Give the preparation type.
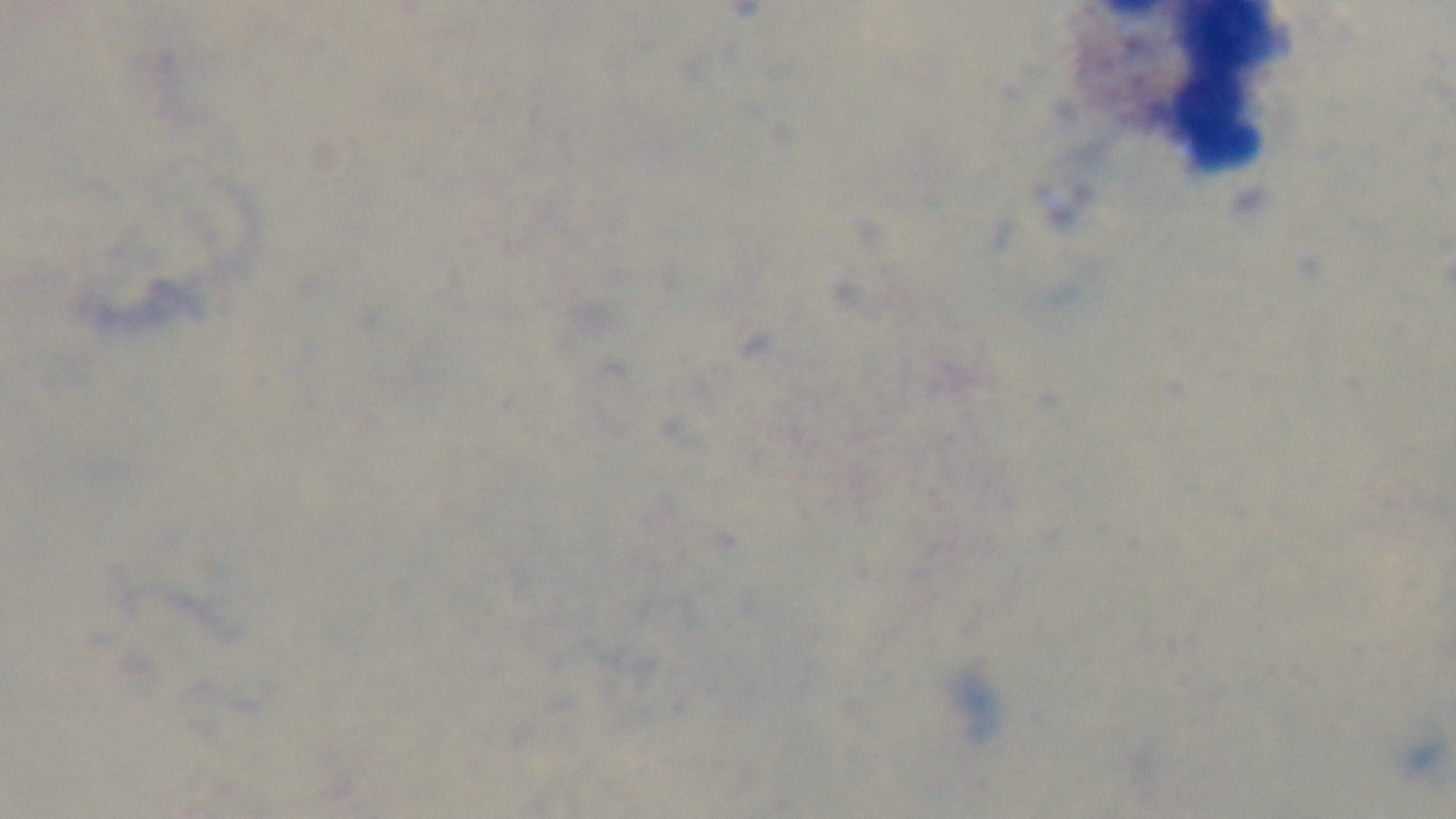
Thick.

capture = mounted 4K digital camera
modality = light microscopy
objective = 100x oil immersion
malaria status = negative
stain = Giemsa
field of view = single